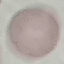

Summary:
  - Result: no malaria parasites detected
  - Capture: smartphone camera at the microscope eyepiece
  - Image type: automatically extracted cell patch, resized to 64 × 64 pixels
  - Stain: Giemsa
  - Preparation: thin smear